Locate every uninfected red blood cell.
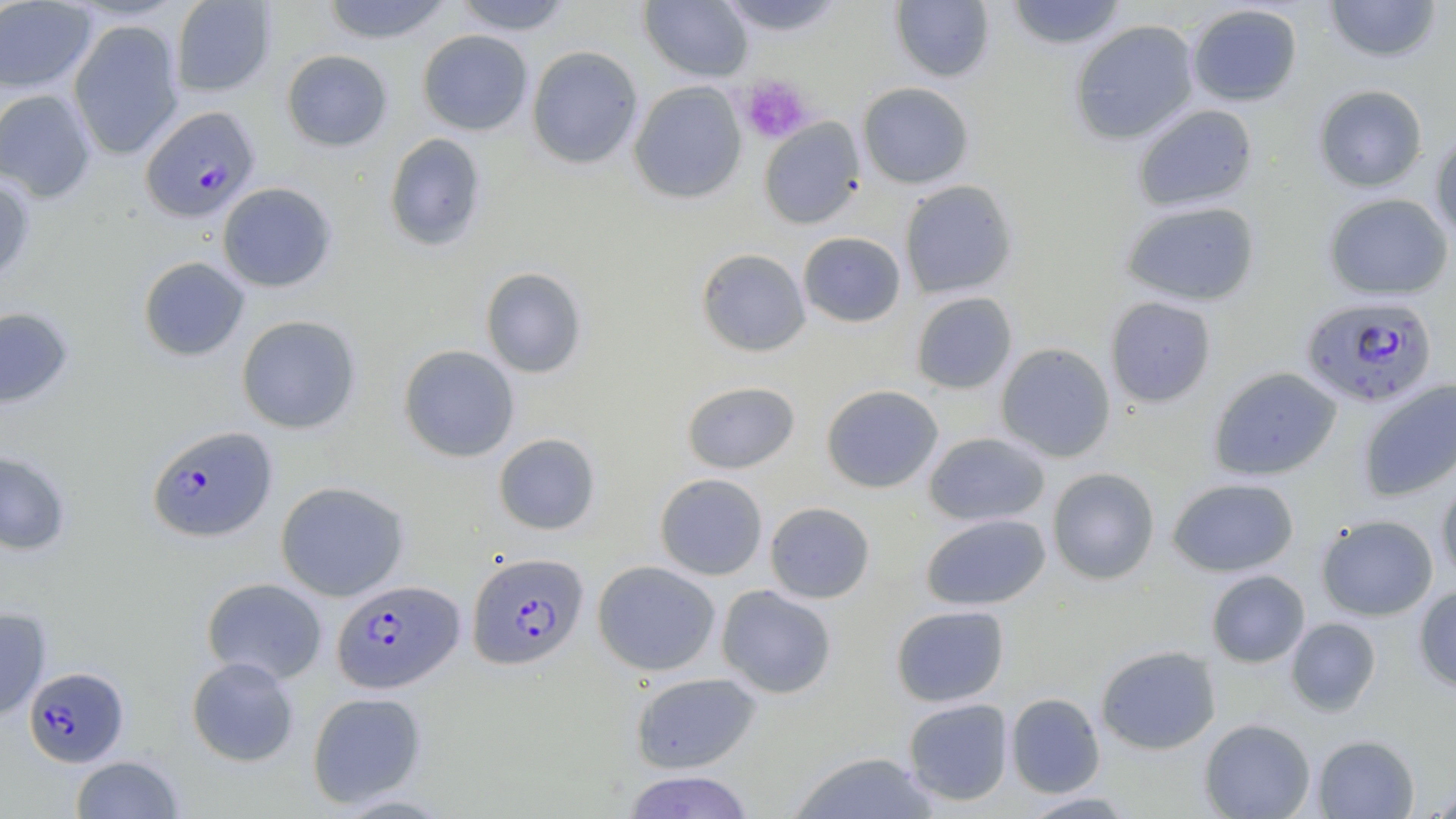

Approximate bounding boxes as (x1, y1, x2, y2) in pixels.
Uninfected red blood cells: (170, 0, 276, 96), (320, 0, 455, 44), (452, 0, 575, 35), (639, 0, 753, 82), (716, 0, 847, 36), (891, 0, 995, 83), (1005, 0, 1128, 50), (1323, 0, 1442, 62), (0, 1, 97, 94), (1187, 3, 1303, 107), (67, 19, 184, 160), (1070, 20, 1199, 144), (417, 30, 533, 136), (526, 45, 644, 169), (281, 49, 393, 152), (629, 81, 747, 204), (857, 82, 974, 189), (1313, 84, 1428, 193), (0, 89, 97, 203), (1132, 104, 1258, 213), (758, 117, 865, 229), (1430, 129, 1456, 242), (384, 133, 488, 252), (0, 174, 35, 288), (899, 179, 1018, 299), (217, 182, 338, 292), (1323, 193, 1453, 300), (1120, 201, 1260, 306), (798, 231, 906, 327), (695, 248, 811, 357), (137, 256, 250, 361), (480, 267, 587, 378), (910, 291, 1018, 395), (1105, 296, 1216, 407), (0, 307, 74, 410), (236, 315, 361, 434), (995, 343, 1116, 462), (398, 344, 520, 462), (1209, 366, 1342, 481), (1219, 377, 1453, 488), (1357, 380, 1456, 503), (681, 381, 800, 474), (821, 384, 944, 493), (923, 432, 1050, 527), (493, 433, 600, 535), (0, 451, 73, 556), (1047, 467, 1160, 585), (1436, 472, 1456, 583), (654, 473, 768, 580), (1167, 477, 1299, 577), (275, 481, 410, 601), (764, 501, 875, 604), (921, 513, 1051, 610), (1316, 514, 1438, 621), (593, 560, 721, 676), (1206, 570, 1310, 668), (201, 577, 328, 685), (716, 584, 837, 698), (1413, 584, 1456, 692), (890, 605, 1010, 707), (0, 607, 52, 720), (1285, 617, 1381, 716), (1095, 645, 1221, 755), (186, 656, 299, 767), (630, 672, 762, 774), (307, 691, 427, 808), (1006, 693, 1105, 798), (903, 698, 1013, 806), (1199, 718, 1316, 819), (1312, 734, 1420, 818), (787, 751, 942, 819), (70, 755, 184, 818), (622, 770, 756, 818), (1424, 782, 1456, 818), (1018, 791, 1137, 818).

Summary:
  - Platelet locations: (739, 74, 814, 144)
  - Plasmodium falciparum-infected red blood cell locations: (140, 106, 260, 223), (1300, 294, 1438, 408), (146, 425, 277, 543), (467, 552, 589, 671), (331, 579, 464, 693), (24, 667, 129, 767)
  - Slide-level diagnosis: Plasmodium falciparum
  - Stain: May-Grünwald-Giemsa
  - Image size: 1456×819 pixels
  - Field of view: one of a larger specimen
  - Modality: light microscopy
  - Magnification: 1000x
  - Preparation: thin blood film